Assess this cell for malaria.
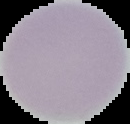
Uninfected.

Image is 130×124 pixels. From a thin blood film. Segmented cell region on a black background.